Describe the morphology of the erythrocytes.
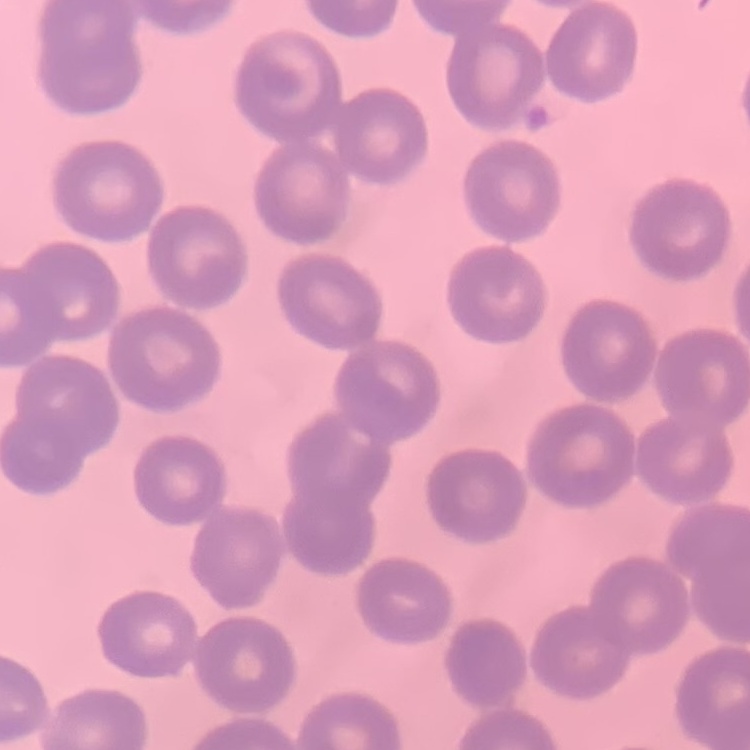

They show no rouleaux formation.

Thin blood smear. Square crop of a larger photomicrograph. Stained with either Field's or Giemsa.